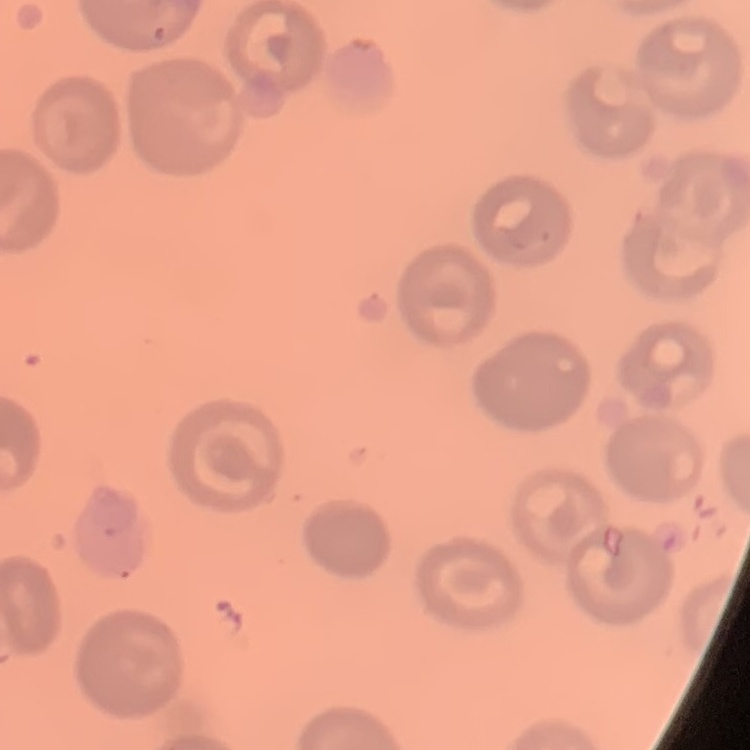

Summary:
  - Erythrocyte morphology: no rouleaux formation
  - Preparation: thin blood smear
  - Stain: Field's or Giemsa
  - Image type: square crop of a larger photomicrograph